Classify this cell by malaria status.
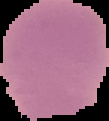
It is uninfected.

image_type: cell region segmented out of the field of view; surrounding area masked to black
preparation: thin blood smear
image_size: 109×121 pixels